Identify the parasite.
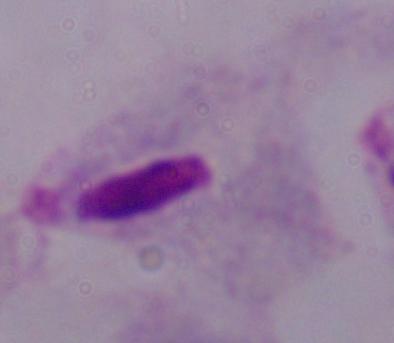

A trichomonad.

Photomicrograph. Captured at 1000x magnification.